Locate every leukocyte (white blood cell).
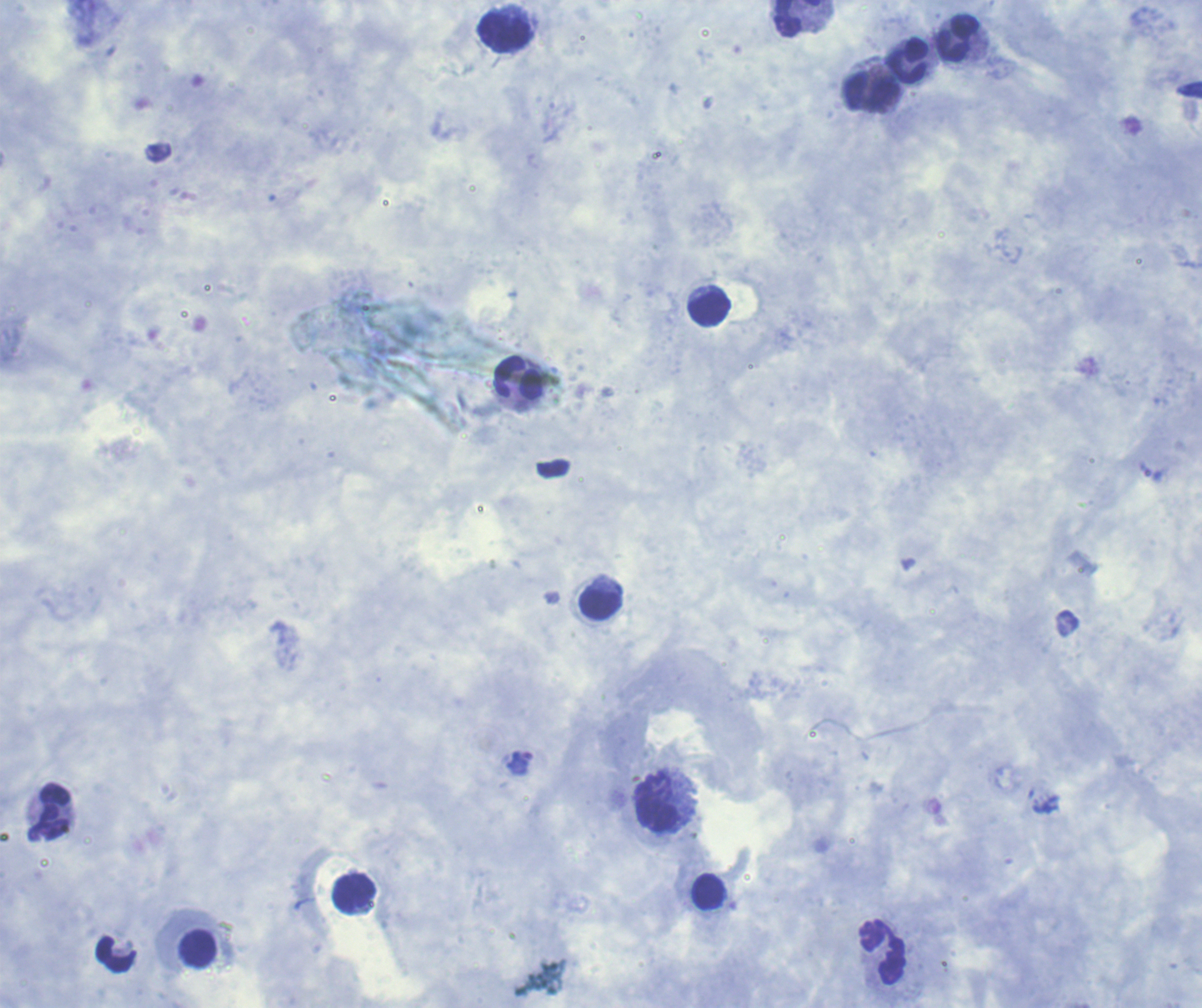

Approximate object centers, in pixels from the top-left corner.
Leukocytes: (x=798, y=18), (x=505, y=33), (x=959, y=38), (x=906, y=61), (x=871, y=91), (x=709, y=307), (x=519, y=377), (x=601, y=603), (x=656, y=802), (x=49, y=812), (x=710, y=891), (x=354, y=893), (x=197, y=949), (x=883, y=952).

Approximate object centers, in pixels from the top-left corner. Trophozoite locations: (x=521, y=763). Single field of view. Result: positive for malaria parasites. Image is 1202×1008 pixels. Background quality: good. Previously used in an actual diagnosis. Coloration quality: good. Romanowsky stain. Thick blood smear. Captured at 100x magnification.